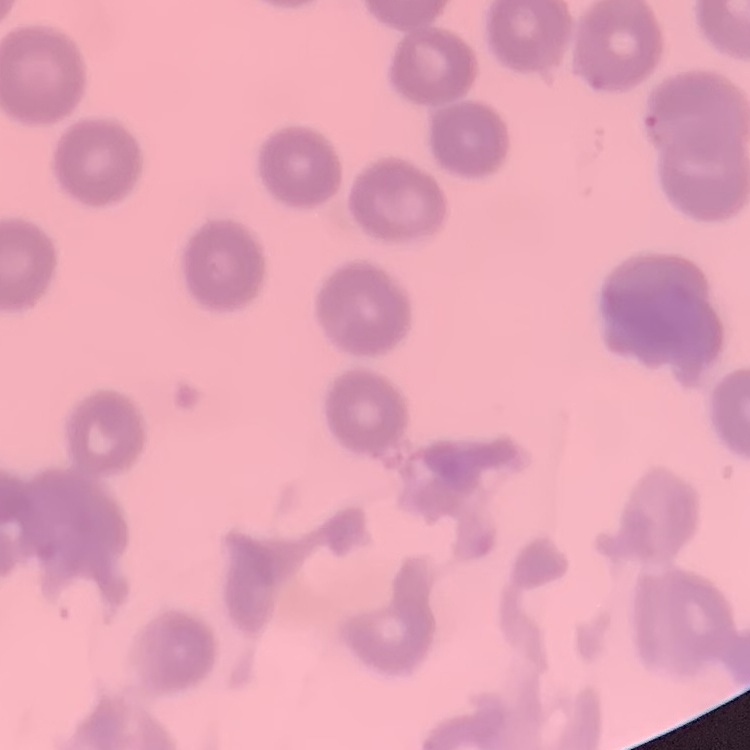

red blood cell morphology = no rouleaux formation
stain = Field's or Giemsa
image type = square crop of a larger photomicrograph
preparation = thin blood film